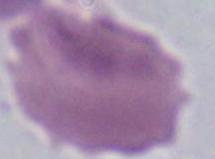 An erythrocyte is shown. 1000x magnification. Photomicrograph.